Classify this cell by malaria status.
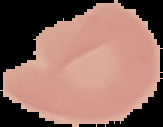
It is uninfected.

Image is 163×127 pixels. From a thin blood smear. Segmented cell region on a black background.